Assess this cell for malaria.
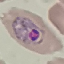

Parasitized.

Giemsa-stained preparation. Photographed with a smartphone camera at the microscope eyepiece. Automatically extracted cell patch, resized to 64 × 64 pixels. Thin blood smear.